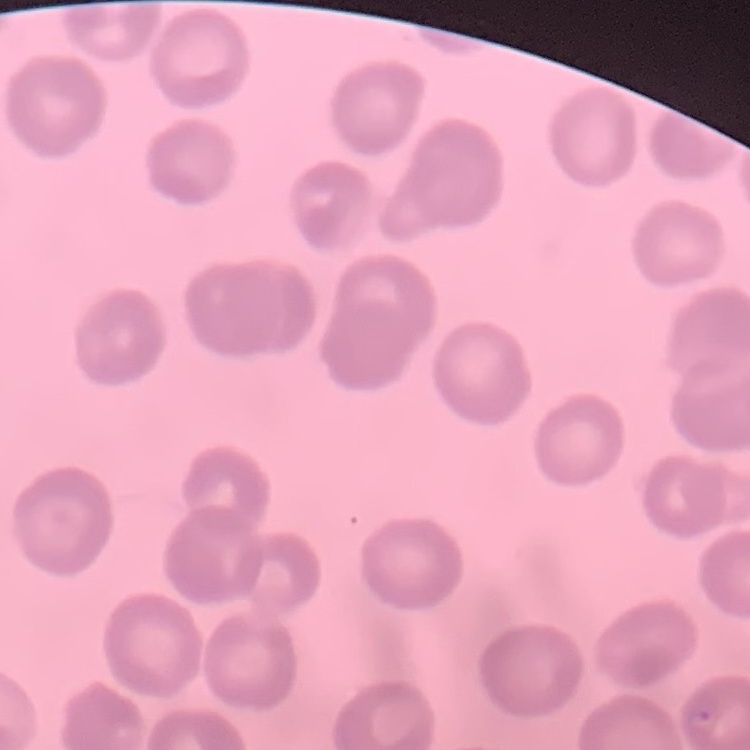

Summary:
  - Red blood cell morphology: no rouleaux formation
  - Preparation: thin peripheral smear
  - Image type: square crop of a larger photomicrograph
  - Stain: Field's or Giemsa